Comment on the morphology of the erythrocytes.
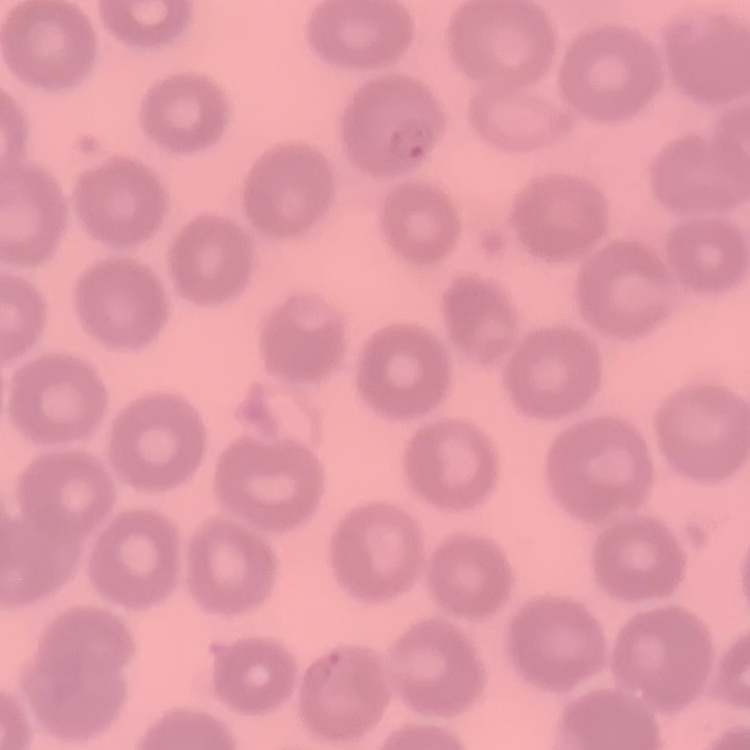

They show no rouleaux formation.

Stained with either Field's or Giemsa. One tile cut from a larger photomicrograph. Thin blood smear.